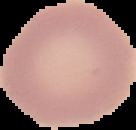
From a thin blood smear. Result: no malaria parasites seen. Segmented cell region on a black background. Image is 136×130 pixels.